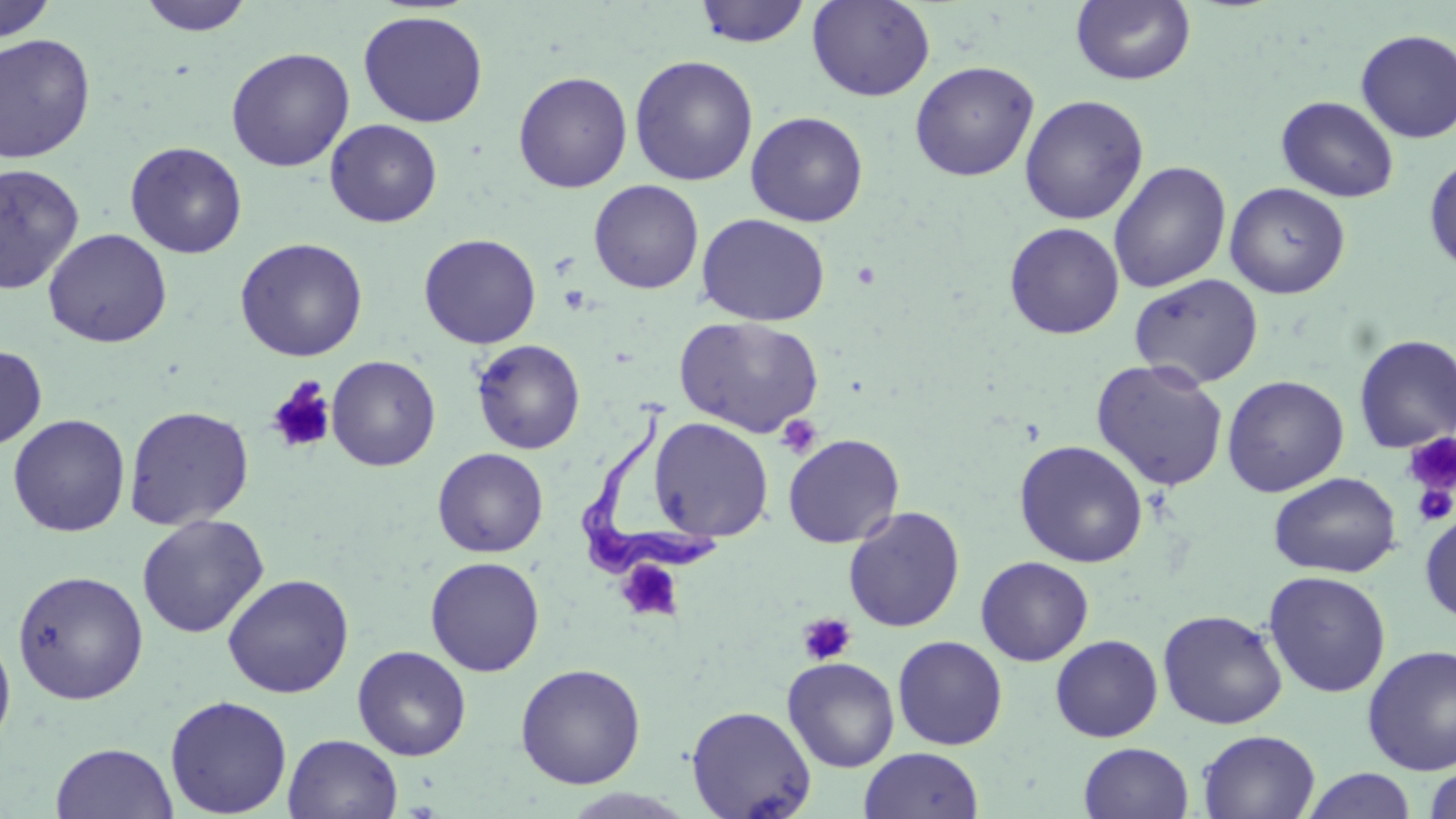
{
  "slide_level_diagnosis": "Trypanosoma brucei",
  "stain": "May-Grünwald-Giemsa",
  "modality": "optical microscopy",
  "field_of_view": "one of a larger specimen",
  "trypanosoma_brucei_locations": "approximate bounding boxes as [x1, y1, x2, y2] in pixels: [577, 409, 714, 583]",
  "preparation": "thin blood smear",
  "uninfected_red_blood_cell_locations": "approximate bounding boxes as [x1, y1, x2, y2] in pixels: [137, 0, 255, 36], [693, 0, 812, 48], [807, 0, 935, 102], [0, 1, 58, 42], [1071, 1, 1197, 86], [357, 10, 488, 127], [1355, 28, 1456, 142], [0, 33, 96, 163], [226, 47, 355, 172], [629, 55, 758, 186], [909, 60, 1039, 181], [513, 71, 633, 193], [1019, 94, 1149, 225], [1276, 95, 1399, 202], [745, 111, 868, 227], [325, 119, 442, 227], [125, 141, 248, 259], [1424, 154, 1456, 277], [1108, 161, 1231, 293], [0, 162, 86, 295], [588, 179, 704, 294], [1224, 182, 1350, 299], [696, 213, 831, 326], [1004, 222, 1125, 339], [43, 228, 172, 348], [418, 233, 541, 349], [235, 237, 368, 362], [1129, 273, 1264, 389], [673, 316, 825, 438], [1353, 334, 1456, 453], [471, 339, 586, 455], [0, 344, 47, 451], [327, 355, 441, 472], [1090, 358, 1229, 493], [1222, 375, 1349, 497], [123, 405, 255, 530], [7, 414, 130, 537], [648, 416, 773, 542], [782, 434, 905, 548], [1014, 440, 1149, 567], [432, 447, 548, 558], [1269, 471, 1401, 578], [843, 506, 965, 632], [1419, 510, 1456, 624], [136, 514, 269, 638], [425, 556, 545, 676], [976, 556, 1094, 666], [12, 570, 149, 704], [1263, 570, 1391, 698], [222, 573, 354, 698], [1157, 609, 1288, 729], [0, 624, 16, 756], [1050, 634, 1163, 742], [892, 635, 1008, 750], [1362, 644, 1456, 776], [352, 645, 471, 760], [782, 656, 900, 773], [515, 663, 646, 789], [164, 695, 292, 818], [685, 704, 817, 819], [1198, 729, 1320, 819], [283, 734, 403, 819], [50, 742, 178, 819], [1079, 742, 1194, 819], [858, 747, 984, 819], [1424, 765, 1456, 819], [1301, 768, 1417, 819]",
  "image_size": "1456×819 pixels",
  "platelet_locations": "approximate bounding boxes as [x1, y1, x2, y2] in pixels: [267, 379, 336, 454], [776, 414, 822, 459], [1403, 431, 1456, 502], [1411, 481, 1455, 527], [616, 558, 684, 621], [798, 613, 857, 666]",
  "magnification": "1000x"
}